Identify the parasite.
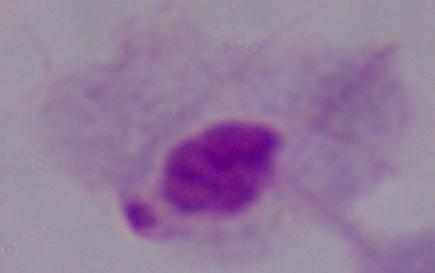

This is a trichomonad.

magnification = 1000x
modality = photomicrograph